Classify this cell by malaria status.
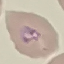
It is parasitized.

Cell patch, automatically extracted from a larger field of view and resized to 64 × 64 pixels. Photographed with a smartphone camera at the microscope eyepiece. Giemsa-stained preparation. Thin smear of blood.